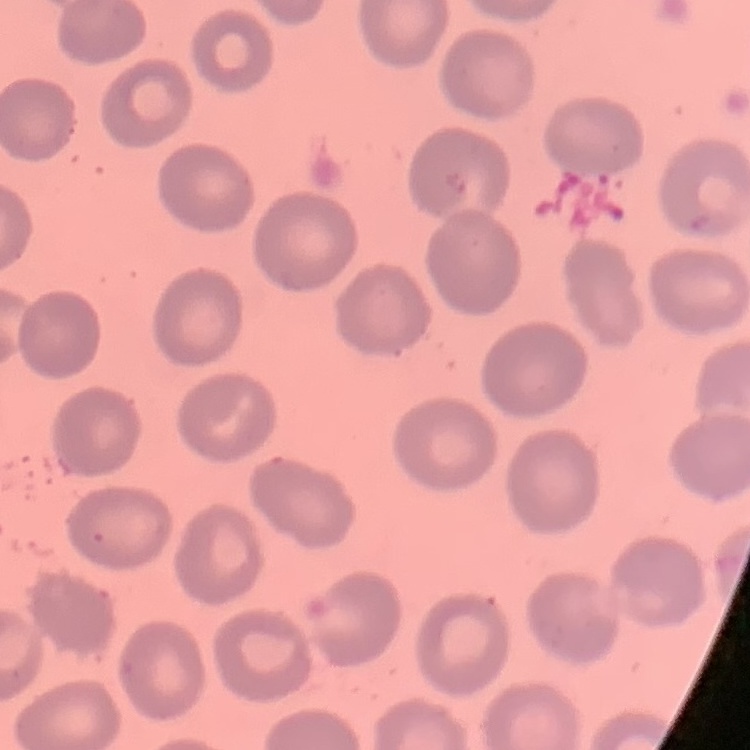

The red blood cells show no rouleaux formation. Stained with either Field's or Giemsa. Thin blood smear. Square crop of a larger photomicrograph.